Give the extent of all uninfected red blood cells.
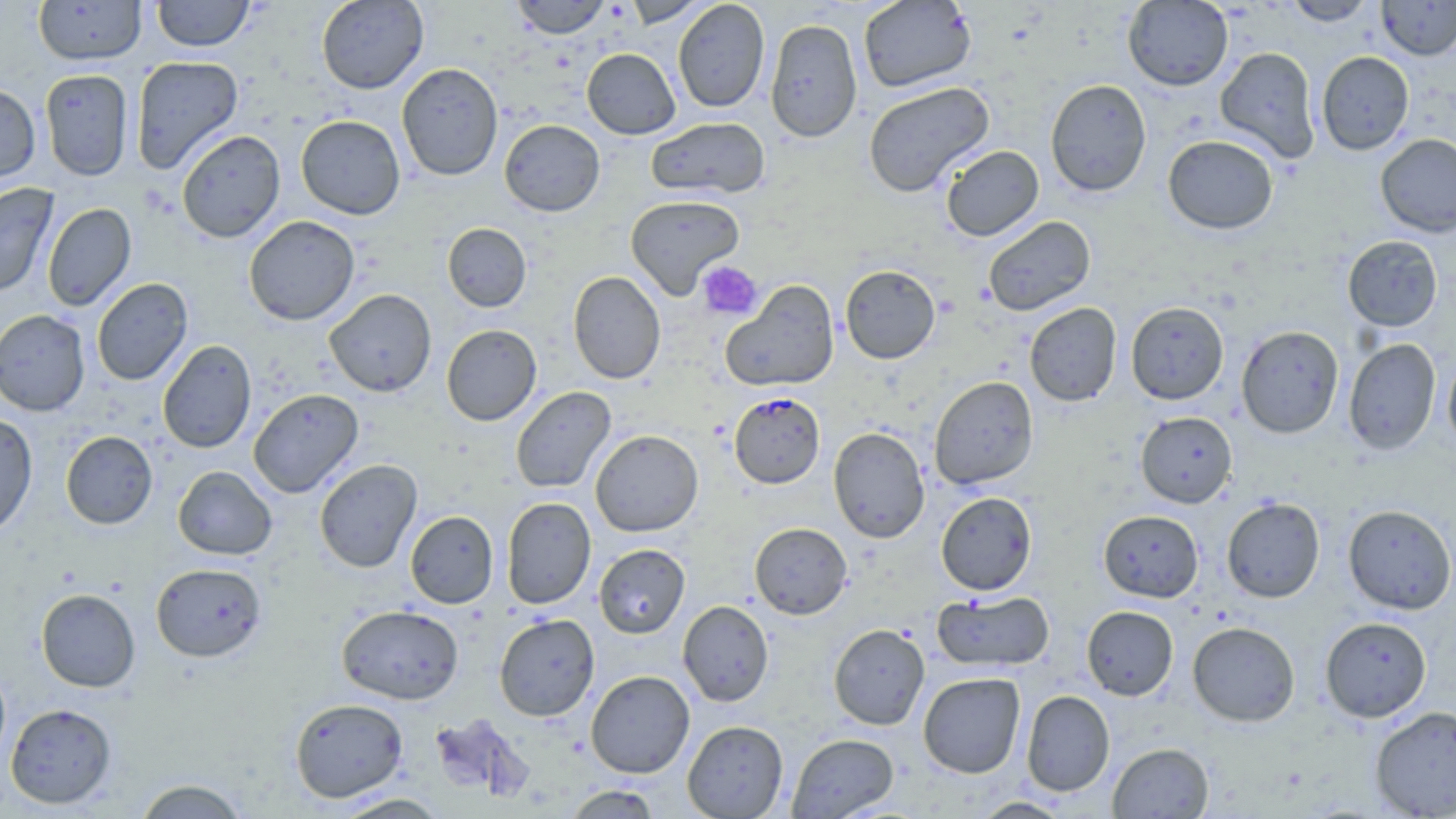
Approximate bounding boxes as (x1, y1, x2, y2) in pixels.
Uninfected red blood cells: (152, 0, 255, 51), (316, 0, 428, 93), (510, 0, 611, 39), (622, 0, 710, 27), (673, 0, 770, 113), (858, 0, 976, 93), (1281, 0, 1378, 26), (1376, 0, 1456, 60), (33, 1, 147, 65), (1122, 1, 1233, 90), (765, 18, 863, 142), (1215, 46, 1321, 163), (582, 48, 681, 139), (1316, 51, 1414, 155), (130, 55, 244, 174), (396, 63, 503, 181), (39, 69, 134, 181), (1045, 79, 1152, 196), (862, 81, 995, 198), (0, 83, 41, 182), (295, 115, 405, 220), (646, 117, 770, 199), (499, 119, 605, 216), (176, 129, 285, 243), (1375, 133, 1456, 237), (1163, 135, 1279, 234), (940, 145, 1044, 241), (0, 183, 58, 298), (624, 194, 745, 299), (42, 203, 136, 311), (244, 215, 360, 325), (983, 215, 1096, 316), (442, 223, 531, 312), (1342, 236, 1442, 331), (840, 264, 940, 364), (568, 271, 666, 384), (92, 278, 193, 386), (720, 280, 839, 392), (324, 289, 436, 397), (1125, 301, 1229, 404), (1024, 303, 1122, 406), (0, 310, 90, 416), (442, 324, 541, 425), (1236, 325, 1344, 438), (1343, 338, 1440, 455), (157, 340, 257, 453), (1442, 352, 1456, 452), (929, 376, 1039, 489), (510, 386, 616, 493), (248, 388, 363, 498), (1135, 411, 1237, 507), (0, 413, 37, 538), (828, 427, 930, 543), (590, 429, 703, 536), (60, 431, 158, 529), (314, 458, 422, 573), (173, 466, 277, 560), (935, 491, 1037, 595), (501, 497, 596, 609), (1221, 497, 1325, 602), (1342, 504, 1456, 614), (1099, 510, 1203, 602), (405, 511, 498, 608), (749, 522, 852, 619), (594, 544, 690, 638), (151, 562, 267, 662), (36, 588, 140, 692), (932, 590, 1054, 673), (678, 600, 774, 706), (337, 604, 464, 704), (1081, 605, 1178, 700), (494, 613, 599, 721), (1320, 616, 1432, 722), (1187, 621, 1300, 726), (828, 624, 930, 730), (586, 670, 695, 778), (918, 672, 1025, 778), (1021, 690, 1115, 796), (290, 698, 408, 802), (5, 702, 117, 809), (1370, 705, 1456, 818), (682, 720, 788, 818), (787, 733, 899, 818), (1107, 742, 1214, 818), (133, 779, 250, 818), (565, 785, 660, 818), (332, 793, 450, 818), (971, 797, 1072, 818).

slide_level_diagnosis: Plasmodium falciparum
image_size: 1456×819 pixels
preparation: thin blood smear
field_of_view: one of a larger specimen
platelet_locations: 'approximate bounding boxes as (x1, y1, x2, y2) in pixels: (697, 260, 763, 320)'
stain: May-Grünwald-Giemsa
plasmodium_falciparum_infected_red_blood_cell_locations: 'approximate bounding boxes as (x1, y1, x2, y2) in pixels: (729, 392, 825, 488)'
magnification: 1000x
modality: light microscopy